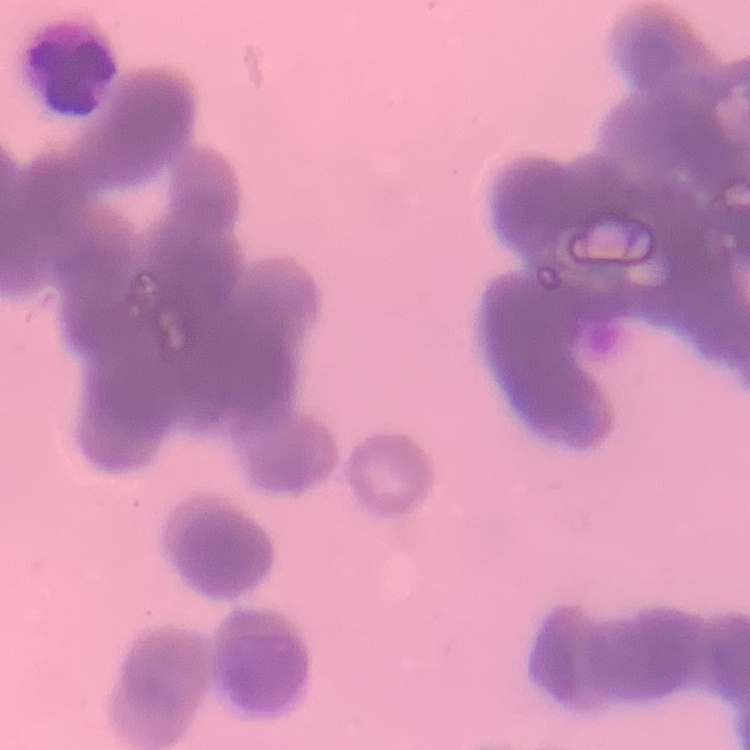
Summary:
  - Erythrocyte morphology: rouleaux formation
  - Image type: one tile cut from a larger photomicrograph
  - Stain: Field's or Giemsa
  - Preparation: thin peripheral smear